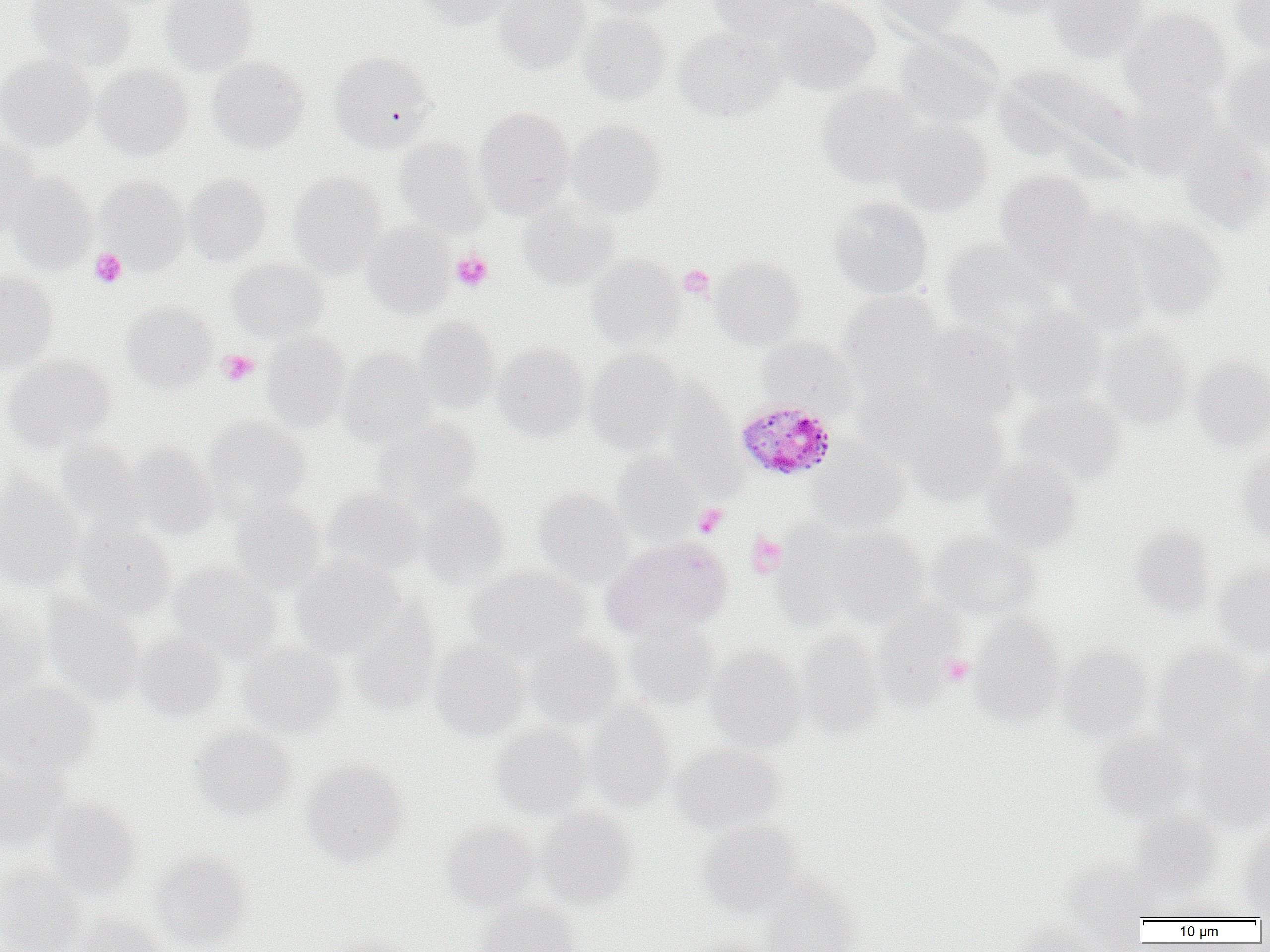

slide_level_diagnosis: Plasmodium malariae
platelet_locations: 'approximate bounding boxes as named x1/y1/x2/y2 corners in pixels: (x1=90, y1=248, x2=127, y2=288), (x1=451, y1=251, x2=493, y2=291), (x1=678, y1=264, x2=715, y2=300), (x1=217, y1=349, x2=260, y2=386), (x1=693, y1=503, x2=728, y2=538), (x1=746, y1=533, x2=787, y2=578), (x1=939, y1=653, x2=974, y2=687)'
plasmodium_malariae_infected_red_blood_cell_locations: 'approximate bounding boxes as named x1/y1/x2/y2 corners in pixels: (x1=735, y1=399, x2=838, y2=481)'
uninfected_red_blood_cell_locations: 'approximate bounding boxes as named x1/y1/x2/y2 corners in pixels: (x1=27, y1=0, x2=136, y2=72), (x1=159, y1=0, x2=260, y2=77), (x1=413, y1=0, x2=511, y2=29), (x1=492, y1=0, x2=591, y2=75), (x1=582, y1=0, x2=682, y2=19), (x1=709, y1=0, x2=822, y2=46), (x1=777, y1=0, x2=881, y2=96), (x1=871, y1=0, x2=972, y2=38), (x1=968, y1=0, x2=1068, y2=19), (x1=1044, y1=0, x2=1149, y2=60), (x1=1230, y1=0, x2=1270, y2=55), (x1=1119, y1=6, x2=1233, y2=109), (x1=577, y1=11, x2=672, y2=106), (x1=674, y1=26, x2=787, y2=121), (x1=894, y1=32, x2=1004, y2=129), (x1=327, y1=50, x2=435, y2=152), (x1=0, y1=52, x2=97, y2=151), (x1=1221, y1=52, x2=1270, y2=155), (x1=207, y1=57, x2=309, y2=153), (x1=92, y1=63, x2=193, y2=160), (x1=817, y1=83, x2=927, y2=188), (x1=1119, y1=85, x2=1220, y2=179), (x1=474, y1=106, x2=576, y2=217), (x1=890, y1=118, x2=994, y2=217), (x1=569, y1=119, x2=667, y2=217), (x1=1177, y1=129, x2=1270, y2=233), (x1=394, y1=137, x2=492, y2=236), (x1=0, y1=138, x2=43, y2=237), (x1=994, y1=169, x2=1098, y2=276), (x1=7, y1=172, x2=97, y2=274), (x1=183, y1=172, x2=272, y2=266), (x1=288, y1=172, x2=386, y2=275), (x1=96, y1=177, x2=191, y2=273), (x1=828, y1=196, x2=934, y2=298), (x1=518, y1=201, x2=621, y2=291), (x1=1058, y1=211, x2=1157, y2=332), (x1=1129, y1=216, x2=1226, y2=320), (x1=361, y1=221, x2=456, y2=318), (x1=939, y1=237, x2=1058, y2=337), (x1=586, y1=254, x2=683, y2=350), (x1=711, y1=254, x2=806, y2=350), (x1=228, y1=257, x2=329, y2=342), (x1=0, y1=271, x2=58, y2=372), (x1=839, y1=289, x2=945, y2=391), (x1=122, y1=301, x2=218, y2=392), (x1=1007, y1=304, x2=1108, y2=404), (x1=414, y1=316, x2=500, y2=413), (x1=917, y1=321, x2=1020, y2=419), (x1=1097, y1=327, x2=1194, y2=428), (x1=262, y1=330, x2=351, y2=430), (x1=756, y1=335, x2=858, y2=416), (x1=493, y1=342, x2=590, y2=441), (x1=340, y1=348, x2=436, y2=446), (x1=585, y1=348, x2=683, y2=452), (x1=2, y1=354, x2=116, y2=452), (x1=1189, y1=355, x2=1270, y2=451), (x1=856, y1=378, x2=958, y2=461), (x1=657, y1=379, x2=737, y2=480), (x1=1013, y1=392, x2=1126, y2=488), (x1=909, y1=410, x2=1011, y2=504), (x1=203, y1=416, x2=311, y2=516), (x1=371, y1=418, x2=481, y2=510), (x1=55, y1=439, x2=148, y2=533), (x1=807, y1=440, x2=910, y2=531), (x1=127, y1=443, x2=218, y2=539), (x1=1237, y1=449, x2=1270, y2=548), (x1=611, y1=451, x2=703, y2=540), (x1=980, y1=456, x2=1085, y2=554), (x1=0, y1=476, x2=84, y2=590), (x1=533, y1=486, x2=633, y2=584), (x1=321, y1=488, x2=427, y2=579), (x1=415, y1=491, x2=510, y2=589), (x1=229, y1=497, x2=327, y2=595), (x1=72, y1=518, x2=176, y2=620), (x1=807, y1=522, x2=931, y2=628), (x1=1129, y1=525, x2=1217, y2=616), (x1=928, y1=531, x2=1042, y2=620), (x1=603, y1=537, x2=732, y2=638), (x1=291, y1=555, x2=405, y2=657), (x1=1213, y1=559, x2=1270, y2=658), (x1=168, y1=562, x2=282, y2=663), (x1=466, y1=565, x2=591, y2=660), (x1=41, y1=594, x2=146, y2=707), (x1=0, y1=600, x2=51, y2=705), (x1=874, y1=600, x2=967, y2=710), (x1=346, y1=603, x2=441, y2=715), (x1=970, y1=614, x2=1065, y2=726), (x1=622, y1=618, x2=717, y2=708), (x1=793, y1=630, x2=886, y2=740), (x1=132, y1=631, x2=228, y2=721), (x1=526, y1=631, x2=625, y2=729), (x1=430, y1=640, x2=531, y2=741), (x1=237, y1=641, x2=346, y2=738), (x1=705, y1=644, x2=808, y2=750), (x1=1055, y1=644, x2=1154, y2=741), (x1=1153, y1=644, x2=1258, y2=740), (x1=1240, y1=662, x2=1269, y2=758), (x1=0, y1=682, x2=100, y2=775), (x1=582, y1=702, x2=676, y2=812), (x1=490, y1=723, x2=594, y2=818), (x1=191, y1=724, x2=297, y2=821), (x1=1191, y1=728, x2=1270, y2=829), (x1=1091, y1=729, x2=1192, y2=819), (x1=672, y1=743, x2=784, y2=833), (x1=0, y1=755, x2=73, y2=851), (x1=300, y1=758, x2=409, y2=865), (x1=6, y1=765, x2=121, y2=873), (x1=45, y1=799, x2=142, y2=897), (x1=535, y1=805, x2=638, y2=908), (x1=1131, y1=806, x2=1222, y2=893), (x1=699, y1=819, x2=803, y2=916), (x1=439, y1=820, x2=540, y2=911), (x1=1238, y1=826, x2=1270, y2=917), (x1=150, y1=851, x2=253, y2=949), (x1=1061, y1=863, x2=1150, y2=943), (x1=0, y1=865, x2=87, y2=952), (x1=760, y1=873, x2=861, y2=952), (x1=1157, y1=893, x2=1244, y2=921), (x1=477, y1=898, x2=579, y2=952), (x1=69, y1=914, x2=169, y2=952), (x1=1012, y1=921, x2=1110, y2=952), (x1=324, y1=933, x2=421, y2=952), (x1=679, y1=933, x2=775, y2=952)'
preparation: thin blood film
magnification: 1000x
image_size: 1270×952 pixels
modality: light microscopy
field_of_view: single